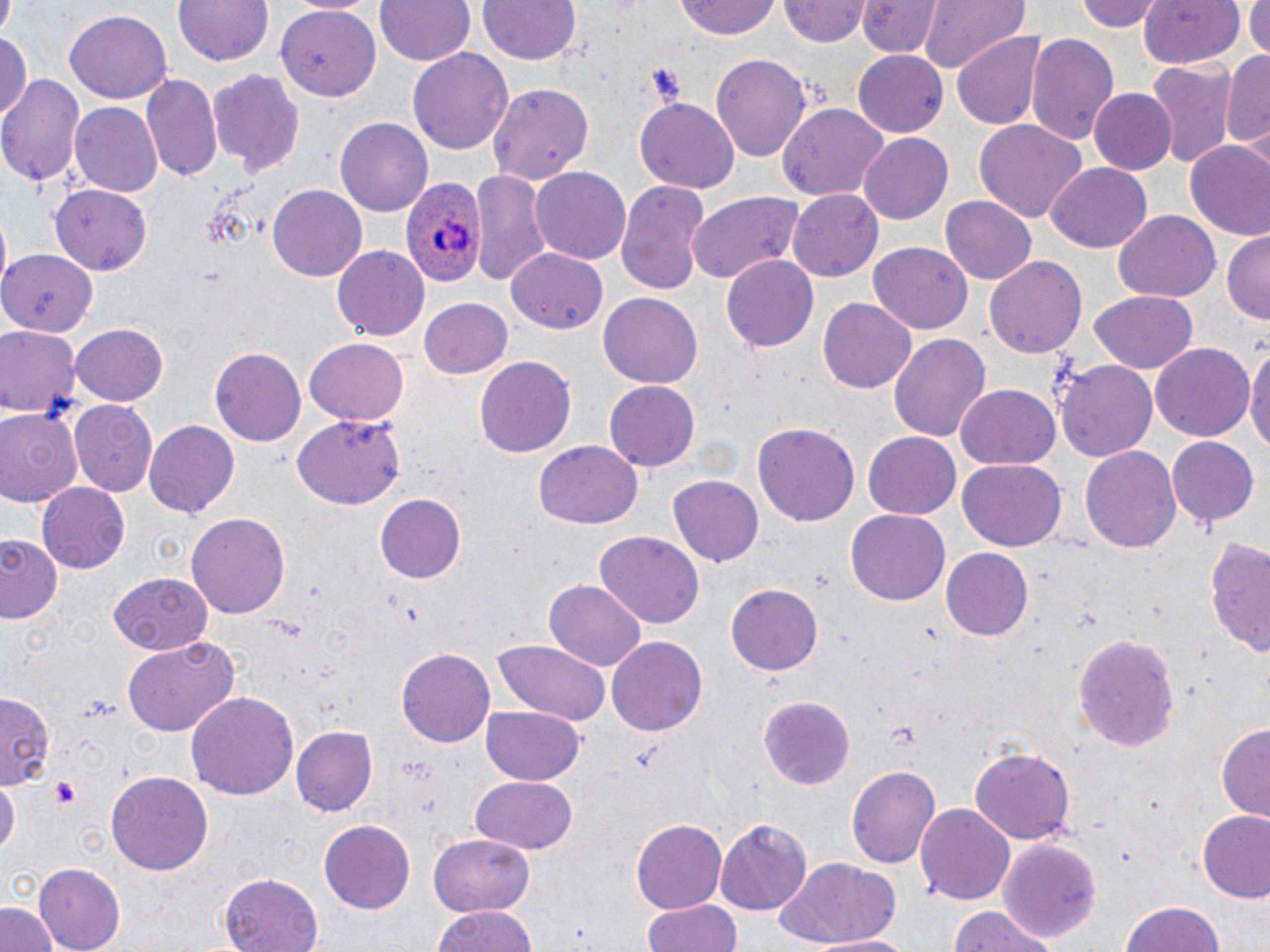
slide_level_diagnosis: Plasmodium ovale
preparation: thin blood smear
plasmodium_ovale_infected_red_blood_cell_locations: 'approximate bounding boxes as [x1, y1, x2, y2] in pixels: [398, 177, 485, 288]'
stain: May-Grünwald-Giemsa
uninfected_red_blood_cell_locations: 'approximate bounding boxes as [x1, y1, x2, y2] in pixels: [172, 0, 276, 70], [377, 0, 474, 66], [473, 0, 584, 66], [673, 0, 782, 40], [858, 0, 943, 59], [919, 0, 1030, 74], [1075, 0, 1164, 33], [779, 1, 871, 48], [1139, 1, 1245, 71], [1242, 2, 1267, 59], [277, 6, 380, 101], [64, 9, 173, 103], [951, 32, 1049, 131], [0, 33, 30, 123], [1025, 33, 1120, 149], [410, 45, 514, 154], [1223, 47, 1270, 154], [854, 51, 948, 137], [710, 53, 813, 162], [1146, 61, 1236, 168], [208, 68, 306, 175], [1, 72, 83, 187], [140, 73, 222, 182], [489, 81, 596, 183], [1089, 88, 1177, 175], [635, 99, 740, 192], [778, 102, 886, 203], [71, 103, 162, 199], [337, 117, 432, 218], [974, 120, 1085, 224], [859, 133, 952, 222], [1184, 139, 1270, 241], [1047, 164, 1150, 251], [532, 167, 631, 265], [470, 168, 555, 287], [615, 179, 713, 294], [49, 184, 154, 274], [266, 184, 367, 282], [788, 190, 883, 282], [686, 192, 811, 285], [939, 195, 1037, 285], [1115, 209, 1221, 300], [1222, 232, 1269, 325], [869, 242, 975, 336], [332, 245, 433, 340], [0, 247, 98, 335], [507, 247, 609, 331], [984, 253, 1088, 359], [722, 254, 818, 350], [600, 291, 704, 389], [1088, 291, 1200, 374], [819, 297, 915, 394], [420, 298, 513, 380], [70, 323, 168, 408], [0, 324, 82, 418], [889, 331, 990, 442], [303, 336, 410, 425], [1246, 343, 1270, 462], [1149, 344, 1255, 444], [210, 346, 306, 447], [475, 355, 577, 458], [1056, 358, 1158, 465], [604, 382, 699, 469], [957, 382, 1060, 468], [70, 400, 159, 498], [0, 409, 82, 509], [291, 413, 404, 509], [144, 420, 242, 517], [753, 423, 859, 527], [864, 429, 961, 516], [1167, 436, 1260, 526], [533, 441, 641, 530], [1082, 444, 1182, 556], [956, 459, 1067, 551], [669, 476, 762, 565], [37, 483, 130, 573], [374, 491, 466, 582], [846, 507, 948, 603], [186, 511, 291, 621], [595, 531, 704, 630], [1, 534, 62, 624], [1204, 536, 1270, 660], [941, 548, 1034, 641], [110, 575, 211, 656], [543, 579, 646, 672], [725, 583, 823, 675], [1074, 632, 1180, 752], [607, 634, 708, 736], [122, 636, 241, 737], [492, 639, 610, 726], [396, 646, 495, 749], [0, 691, 54, 788], [187, 691, 301, 801], [755, 694, 855, 788], [481, 703, 584, 784], [1217, 723, 1270, 822], [294, 726, 377, 816], [969, 743, 1077, 844], [846, 763, 941, 868], [104, 769, 213, 874], [470, 775, 580, 854], [1, 779, 18, 861], [916, 801, 1014, 908], [1196, 809, 1270, 901], [630, 819, 726, 915], [715, 819, 811, 913], [319, 821, 415, 911], [428, 834, 535, 916], [1000, 838, 1102, 943], [773, 856, 905, 945], [34, 862, 127, 952], [219, 874, 324, 952], [641, 899, 743, 952], [1117, 899, 1227, 952], [0, 902, 60, 952], [432, 904, 538, 952], [946, 908, 1059, 952], [812, 933, 917, 951]'
field_of_view: one of a larger specimen
magnification: 1000x
modality: optical microscopy
platelet_locations: 'approximate bounding boxes as [x1, y1, x2, y2] in pixels: [50, 776, 84, 810]'
image_size: 1270×952 pixels